Outline each blood parasite and name the species.
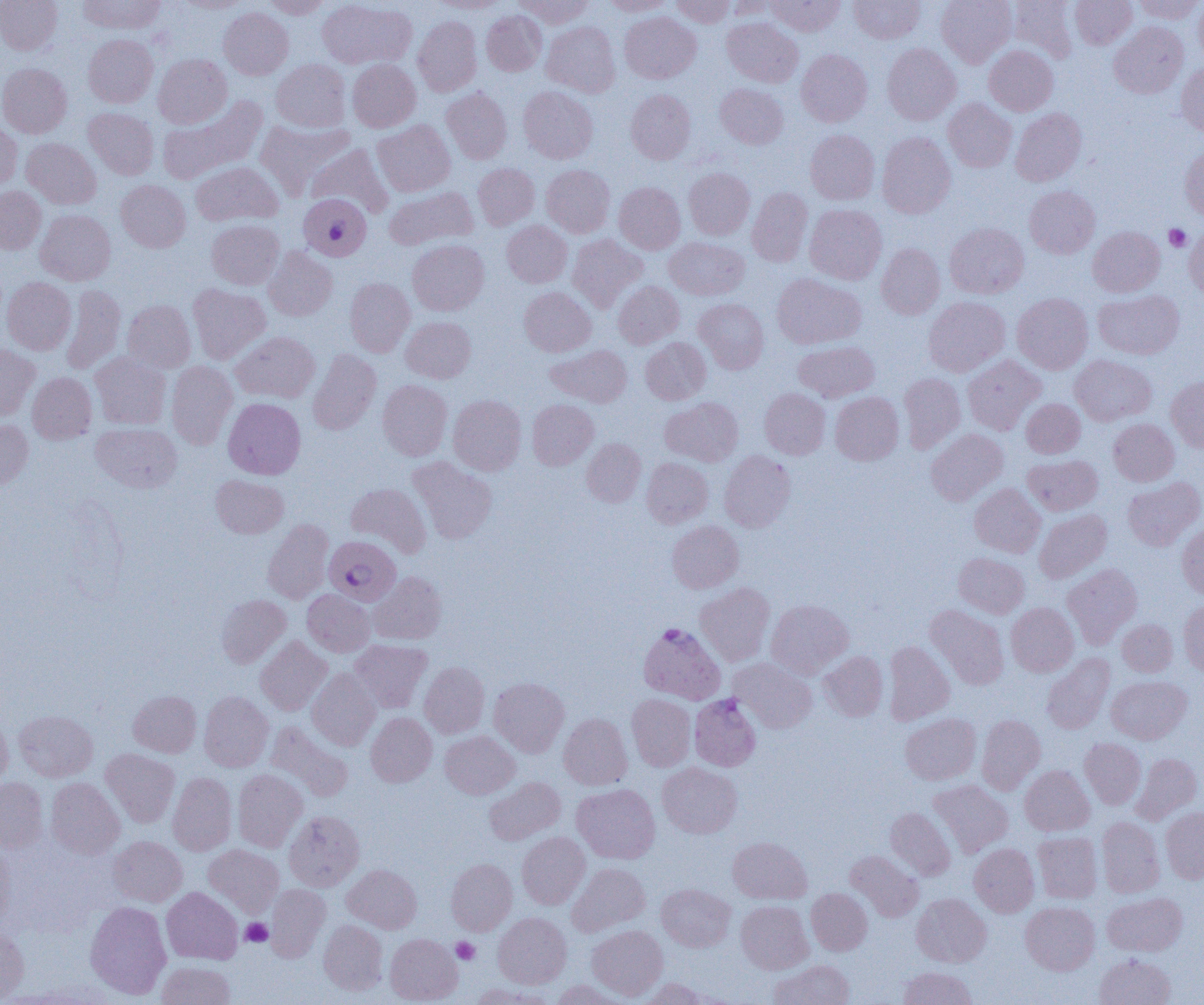

Approximate bounding boxes as named x1/y1/x2/y2 corners in pixels.
Plasmodium falciparum-infected red blood cells: (x1=298, y1=193, x2=371, y2=261), (x1=325, y1=537, x2=404, y2=605), (x1=638, y1=622, x2=726, y2=703), (x1=689, y1=694, x2=761, y2=771).
No Plasmodium ovale, Plasmodium malariae, Plasmodium vivax, Babesia divergens, or Trypanosoma brucei observed.

slide-level diagnosis = Plasmodium falciparum
image size = 1204×1005 pixels
preparation = thin blood film
platelet locations = approximate bounding boxes as named x1/y1/x2/y2 corners in pixels: (x1=1164, y1=224, x2=1191, y2=251), (x1=240, y1=918, x2=273, y2=946), (x1=452, y1=937, x2=480, y2=964)
field of view = single
uninfected red blood cell locations = approximate bounding boxes as named x1/y1/x2/y2 corners in pixels: (x1=0, y1=0, x2=62, y2=55), (x1=77, y1=0, x2=165, y2=34), (x1=174, y1=0, x2=253, y2=13), (x1=262, y1=0, x2=331, y2=18), (x1=317, y1=0, x2=416, y2=70), (x1=514, y1=0, x2=595, y2=27), (x1=600, y1=0, x2=675, y2=16), (x1=670, y1=0, x2=734, y2=27), (x1=724, y1=0, x2=777, y2=20), (x1=766, y1=0, x2=845, y2=36), (x1=849, y1=0, x2=925, y2=44), (x1=936, y1=0, x2=1016, y2=67), (x1=1009, y1=0, x2=1078, y2=63), (x1=1070, y1=0, x2=1136, y2=49), (x1=1134, y1=0, x2=1203, y2=23), (x1=1194, y1=0, x2=1204, y2=68), (x1=429, y1=1, x2=507, y2=13), (x1=218, y1=7, x2=293, y2=79), (x1=481, y1=11, x2=546, y2=76), (x1=620, y1=12, x2=701, y2=83), (x1=413, y1=16, x2=482, y2=96), (x1=722, y1=17, x2=802, y2=87), (x1=541, y1=21, x2=620, y2=97), (x1=1109, y1=22, x2=1188, y2=98), (x1=83, y1=34, x2=158, y2=107), (x1=882, y1=43, x2=960, y2=124), (x1=985, y1=45, x2=1058, y2=115), (x1=796, y1=49, x2=872, y2=127), (x1=153, y1=53, x2=232, y2=128), (x1=271, y1=59, x2=351, y2=131), (x1=347, y1=60, x2=420, y2=132), (x1=0, y1=63, x2=72, y2=138), (x1=1177, y1=63, x2=1204, y2=136), (x1=715, y1=84, x2=788, y2=149), (x1=518, y1=86, x2=598, y2=164), (x1=441, y1=88, x2=512, y2=164), (x1=626, y1=90, x2=696, y2=164), (x1=158, y1=95, x2=267, y2=185), (x1=943, y1=98, x2=1016, y2=172), (x1=83, y1=107, x2=158, y2=179), (x1=1010, y1=108, x2=1086, y2=186), (x1=255, y1=119, x2=356, y2=198), (x1=0, y1=120, x2=22, y2=191), (x1=372, y1=120, x2=455, y2=196), (x1=805, y1=129, x2=879, y2=204), (x1=877, y1=132, x2=956, y2=218), (x1=21, y1=138, x2=100, y2=209), (x1=306, y1=143, x2=394, y2=217), (x1=1180, y1=146, x2=1204, y2=220), (x1=191, y1=161, x2=283, y2=227), (x1=473, y1=163, x2=539, y2=229), (x1=541, y1=165, x2=615, y2=237), (x1=684, y1=167, x2=754, y2=239), (x1=116, y1=180, x2=190, y2=252), (x1=614, y1=182, x2=685, y2=254), (x1=0, y1=186, x2=45, y2=254), (x1=1024, y1=186, x2=1100, y2=258), (x1=384, y1=187, x2=478, y2=249), (x1=747, y1=187, x2=812, y2=266), (x1=805, y1=204, x2=887, y2=284), (x1=35, y1=209, x2=116, y2=285), (x1=207, y1=219, x2=284, y2=289), (x1=502, y1=220, x2=572, y2=287), (x1=945, y1=223, x2=1028, y2=299), (x1=1088, y1=226, x2=1164, y2=297), (x1=1184, y1=227, x2=1204, y2=300), (x1=567, y1=233, x2=647, y2=312), (x1=664, y1=237, x2=749, y2=300), (x1=408, y1=239, x2=489, y2=315), (x1=876, y1=243, x2=945, y2=319), (x1=263, y1=247, x2=337, y2=320), (x1=772, y1=273, x2=866, y2=349), (x1=2, y1=277, x2=76, y2=355), (x1=345, y1=277, x2=415, y2=357), (x1=613, y1=280, x2=684, y2=348), (x1=187, y1=283, x2=270, y2=364), (x1=60, y1=285, x2=125, y2=374), (x1=519, y1=286, x2=596, y2=356), (x1=1094, y1=290, x2=1183, y2=359), (x1=1013, y1=293, x2=1093, y2=374), (x1=924, y1=297, x2=1009, y2=376), (x1=693, y1=298, x2=768, y2=373), (x1=123, y1=300, x2=196, y2=372), (x1=401, y1=316, x2=475, y2=383), (x1=231, y1=331, x2=320, y2=403), (x1=641, y1=337, x2=711, y2=404), (x1=794, y1=340, x2=879, y2=402), (x1=0, y1=343, x2=39, y2=419), (x1=546, y1=345, x2=632, y2=407), (x1=308, y1=349, x2=381, y2=435), (x1=90, y1=352, x2=171, y2=430), (x1=962, y1=355, x2=1046, y2=435), (x1=1070, y1=355, x2=1156, y2=426), (x1=167, y1=361, x2=237, y2=449), (x1=27, y1=372, x2=97, y2=444), (x1=899, y1=373, x2=965, y2=452), (x1=1166, y1=375, x2=1204, y2=452), (x1=378, y1=379, x2=452, y2=460), (x1=760, y1=388, x2=830, y2=459), (x1=830, y1=391, x2=903, y2=465), (x1=448, y1=395, x2=526, y2=475), (x1=661, y1=397, x2=743, y2=466), (x1=223, y1=398, x2=305, y2=479), (x1=527, y1=399, x2=598, y2=469), (x1=1021, y1=399, x2=1085, y2=458), (x1=0, y1=419, x2=33, y2=491), (x1=1108, y1=419, x2=1179, y2=485), (x1=91, y1=422, x2=182, y2=492), (x1=926, y1=428, x2=1008, y2=504), (x1=582, y1=438, x2=646, y2=507), (x1=719, y1=450, x2=795, y2=532), (x1=1022, y1=455, x2=1103, y2=515), (x1=407, y1=456, x2=497, y2=544), (x1=642, y1=458, x2=713, y2=527), (x1=211, y1=475, x2=288, y2=538), (x1=1122, y1=476, x2=1204, y2=550), (x1=345, y1=482, x2=431, y2=557), (x1=970, y1=483, x2=1046, y2=557), (x1=1034, y1=509, x2=1111, y2=583), (x1=262, y1=519, x2=334, y2=604), (x1=667, y1=521, x2=743, y2=593), (x1=1177, y1=523, x2=1204, y2=600), (x1=954, y1=552, x2=1029, y2=617), (x1=1063, y1=563, x2=1142, y2=647), (x1=369, y1=571, x2=447, y2=644), (x1=695, y1=582, x2=775, y2=666), (x1=302, y1=589, x2=374, y2=656), (x1=216, y1=594, x2=291, y2=668), (x1=766, y1=599, x2=853, y2=678), (x1=1178, y1=601, x2=1204, y2=677), (x1=1006, y1=603, x2=1079, y2=676), (x1=925, y1=604, x2=1009, y2=689), (x1=1117, y1=619, x2=1177, y2=676), (x1=256, y1=636, x2=331, y2=715), (x1=349, y1=639, x2=432, y2=713), (x1=883, y1=641, x2=955, y2=725), (x1=819, y1=651, x2=887, y2=721), (x1=1042, y1=654, x2=1115, y2=734), (x1=729, y1=658, x2=816, y2=733), (x1=419, y1=662, x2=489, y2=738), (x1=307, y1=668, x2=380, y2=750), (x1=1106, y1=675, x2=1191, y2=744), (x1=488, y1=677, x2=569, y2=757), (x1=128, y1=690, x2=201, y2=757), (x1=199, y1=692, x2=273, y2=771), (x1=627, y1=694, x2=696, y2=771), (x1=0, y1=709, x2=12, y2=788), (x1=14, y1=709, x2=98, y2=781), (x1=366, y1=712, x2=437, y2=786), (x1=559, y1=713, x2=632, y2=790), (x1=900, y1=713, x2=981, y2=785), (x1=976, y1=714, x2=1045, y2=795), (x1=266, y1=721, x2=353, y2=801), (x1=440, y1=731, x2=519, y2=799), (x1=1079, y1=738, x2=1146, y2=809), (x1=100, y1=749, x2=180, y2=828), (x1=1131, y1=753, x2=1202, y2=825), (x1=658, y1=763, x2=742, y2=838), (x1=1020, y1=765, x2=1094, y2=836), (x1=233, y1=769, x2=307, y2=852), (x1=168, y1=773, x2=236, y2=855), (x1=484, y1=777, x2=565, y2=845), (x1=0, y1=778, x2=48, y2=853), (x1=46, y1=778, x2=125, y2=859), (x1=928, y1=780, x2=1013, y2=858), (x1=572, y1=784, x2=660, y2=864), (x1=885, y1=807, x2=955, y2=880), (x1=1161, y1=807, x2=1204, y2=883), (x1=284, y1=811, x2=364, y2=891), (x1=1097, y1=817, x2=1164, y2=897), (x1=1033, y1=831, x2=1102, y2=903), (x1=517, y1=832, x2=590, y2=909), (x1=108, y1=836, x2=187, y2=906), (x1=728, y1=836, x2=812, y2=904), (x1=0, y1=838, x2=16, y2=929), (x1=969, y1=843, x2=1039, y2=917), (x1=204, y1=845, x2=283, y2=916), (x1=846, y1=850, x2=924, y2=921), (x1=446, y1=858, x2=517, y2=935), (x1=567, y1=863, x2=650, y2=937), (x1=342, y1=864, x2=422, y2=933), (x1=656, y1=883, x2=735, y2=951), (x1=265, y1=884, x2=330, y2=962), (x1=162, y1=887, x2=243, y2=964), (x1=807, y1=888, x2=872, y2=955), (x1=1102, y1=892, x2=1188, y2=957), (x1=912, y1=893, x2=991, y2=967), (x1=85, y1=901, x2=171, y2=999), (x1=736, y1=901, x2=813, y2=973), (x1=1021, y1=902, x2=1100, y2=975), (x1=493, y1=912, x2=571, y2=988), (x1=319, y1=920, x2=387, y2=995), (x1=587, y1=925, x2=667, y2=1000), (x1=0, y1=927, x2=29, y2=1003), (x1=385, y1=933, x2=462, y2=1004), (x1=1094, y1=953, x2=1176, y2=1005), (x1=769, y1=959, x2=854, y2=1005), (x1=156, y1=961, x2=235, y2=1005), (x1=899, y1=967, x2=977, y2=1005), (x1=640, y1=978, x2=711, y2=1005), (x1=551, y1=979, x2=628, y2=1005), (x1=470, y1=984, x2=552, y2=1005)
modality = optical microscopy
magnification = 1000x